Report the malaria status of this cell.
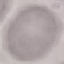

It is uninfected.

Summary:
  - Image type: automatically extracted cell patch, resized to 64 × 64 pixels
  - Capture: smartphone camera at the microscope eyepiece
  - Stain: Giemsa
  - Preparation: thin blood film